Locate and identify every blood parasite.
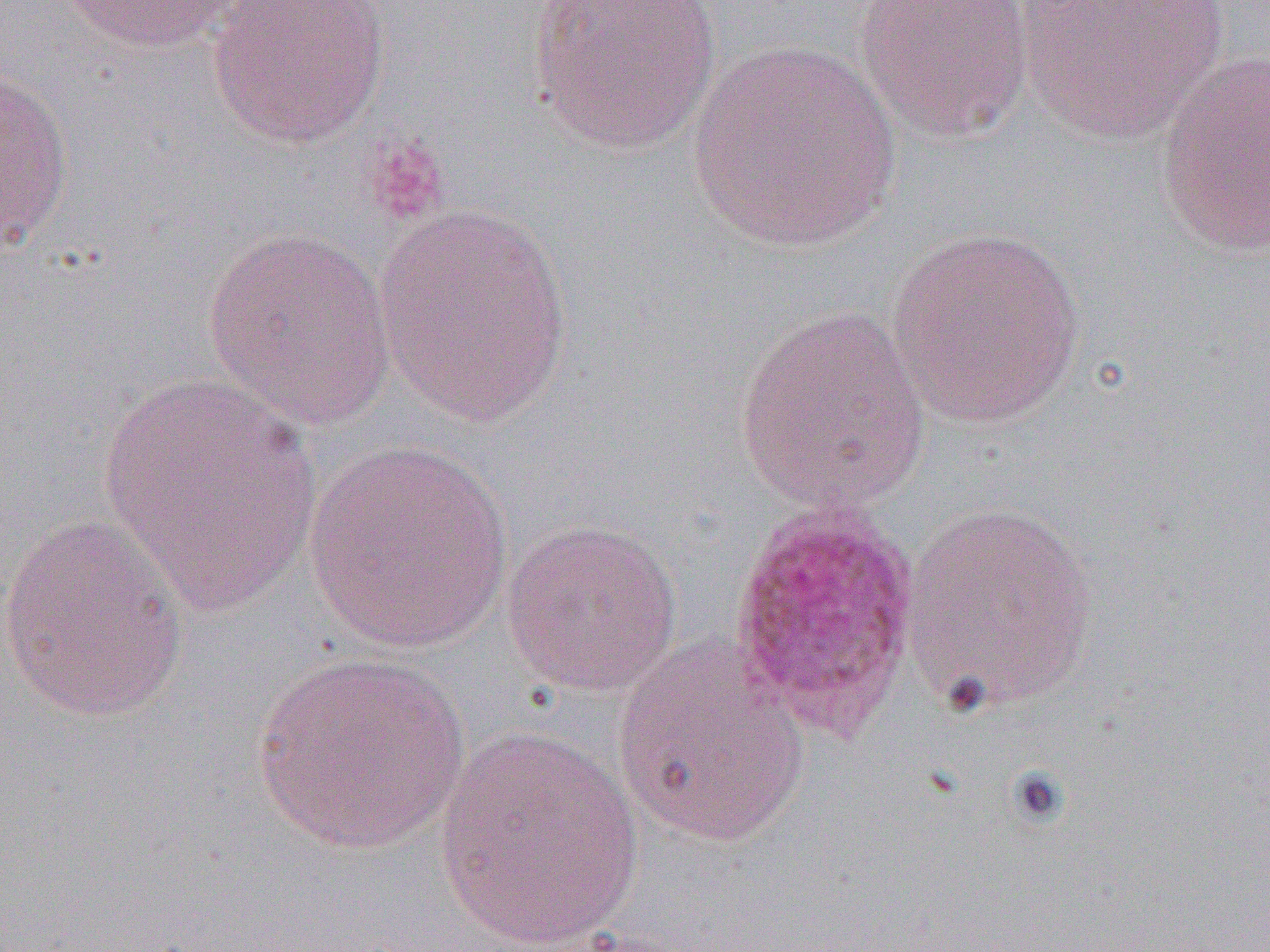

Approximate bounding boxes as named x1/y1/x2/y2 corners in pixels.
Plasmodium ovale-infected red blood cells: (x1=726, y1=505, x2=923, y2=742).
No Plasmodium falciparum, Plasmodium malariae, Plasmodium vivax, Babesia divergens, or Trypanosoma brucei observed.

Summary:
  - Platelet locations: (x1=364, y1=133, x2=450, y2=227)
  - Uninfected red blood cell locations: (x1=56, y1=0, x2=247, y2=54), (x1=205, y1=0, x2=390, y2=149), (x1=527, y1=0, x2=723, y2=157), (x1=855, y1=0, x2=1036, y2=143), (x1=1015, y1=0, x2=1230, y2=144), (x1=687, y1=39, x2=906, y2=254), (x1=1154, y1=53, x2=1270, y2=260), (x1=0, y1=62, x2=75, y2=255), (x1=374, y1=203, x2=575, y2=426), (x1=201, y1=225, x2=397, y2=430), (x1=886, y1=226, x2=1088, y2=428), (x1=734, y1=306, x2=932, y2=513), (x1=99, y1=372, x2=322, y2=617), (x1=302, y1=441, x2=513, y2=653), (x1=900, y1=499, x2=1100, y2=715), (x1=1, y1=511, x2=189, y2=723), (x1=501, y1=518, x2=683, y2=698), (x1=613, y1=636, x2=810, y2=848), (x1=251, y1=653, x2=470, y2=856), (x1=434, y1=726, x2=644, y2=951)
  - Slide-level diagnosis: Plasmodium ovale
  - Preparation: thin blood film
  - Field of view: one of a larger specimen
  - Magnification: 1000x
  - Modality: light microscopy
  - Image size: 1270×952 pixels